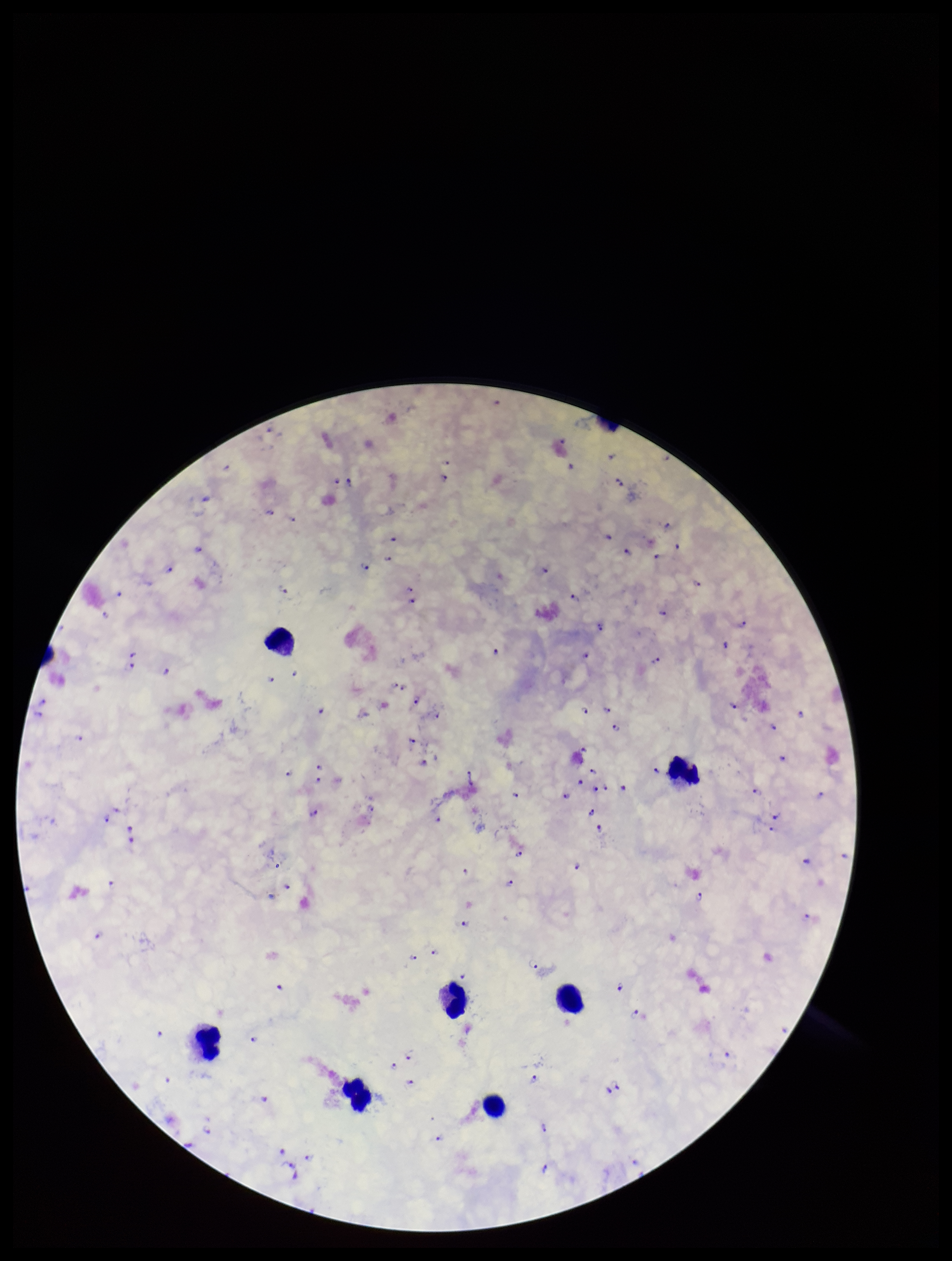
Summary:
  - Stain: Giemsa
  - Capture: smartphone photograph through the microscope eyepiece
  - Leukocyte count: 7
  - Image size: 952×1261 pixels
  - Patient malaria status: infected
  - Plasmodium parasites: seen
  - Species reported for this patient: Plasmodium falciparum
  - Preparation: thick
  - Parasite count: 138
  - Field of view: single